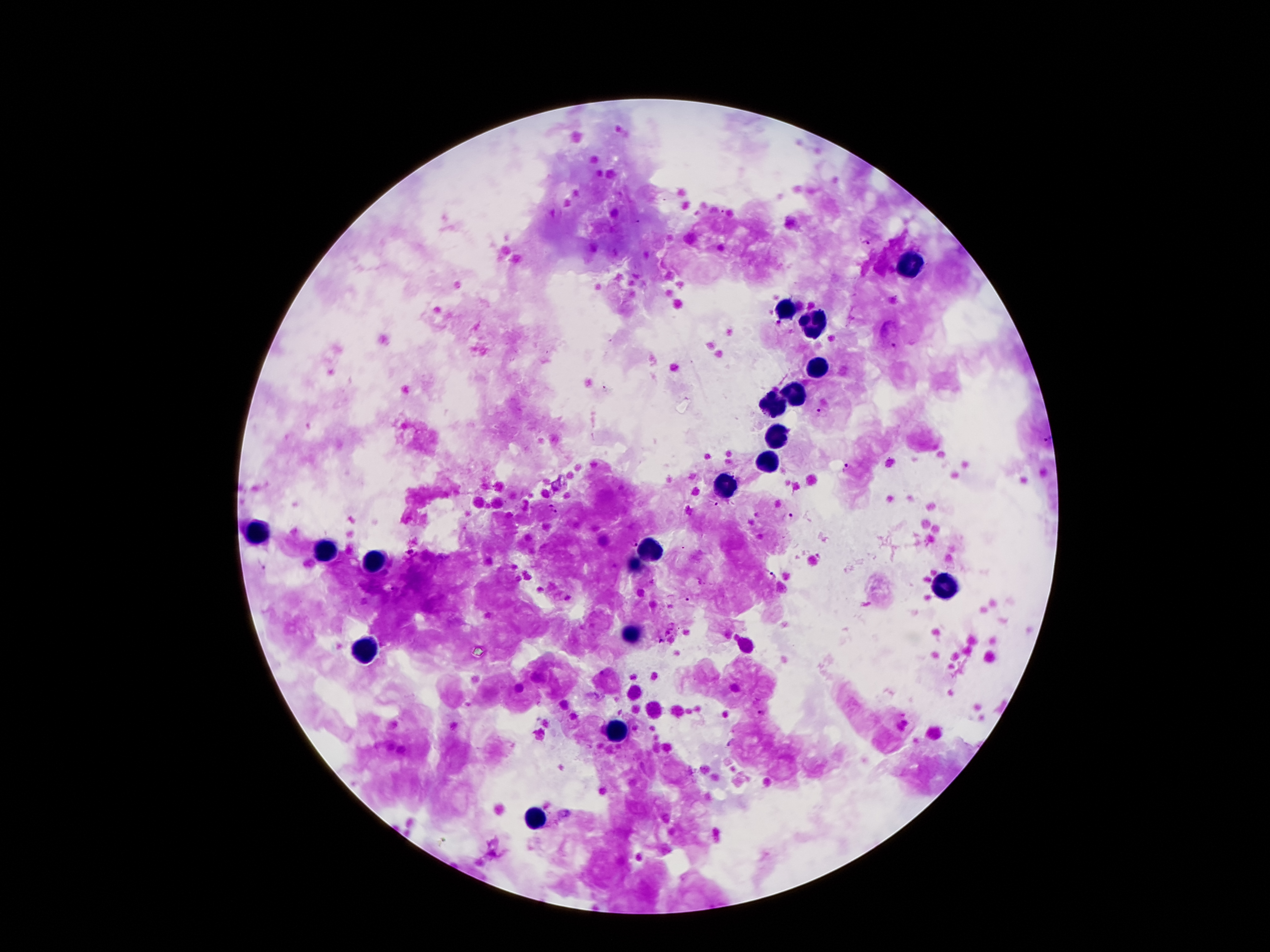

malaria_parasite_locations: 'approximate object centers, in pixels from the top-left corner: (x=723, y=212), (x=636, y=224), (x=865, y=242), (x=778, y=323), (x=893, y=345), (x=604, y=389), (x=822, y=412), (x=1048, y=439), (x=848, y=469), (x=714, y=504), (x=552, y=509), (x=787, y=516), (x=633, y=544), (x=260, y=564), (x=770, y=575), (x=395, y=588), (x=690, y=598), (x=662, y=641), (x=762, y=713), (x=731, y=743)'
leukocyte_locations: 'approximate object centers, in pixels from the top-left corner: (x=912, y=264), (x=785, y=312), (x=817, y=323), (x=819, y=371), (x=796, y=396), (x=776, y=405), (x=778, y=441), (x=767, y=464), (x=721, y=489), (x=258, y=532), (x=651, y=552), (x=326, y=555), (x=374, y=561), (x=637, y=564), (x=944, y=586), (x=633, y=639), (x=365, y=652), (x=617, y=732), (x=533, y=820)'
magnification: 100x
stain: Giemsa
field_of_view: single
capture: smartphone camera through the microscope eyepiece
image_size: 1270×952 pixels
preparation: thick blood film
patient_malaria_status: positive for Plasmodium falciparum